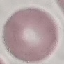

malaria_status: uninfected
image_type: automatically extracted cell patch, resized to 64 × 64 pixels
preparation: thin blood smear
stain: Giemsa
capture: smartphone camera at the microscope eyepiece